Give the extent of all Plasmodium falciparum-infected red blood cells.
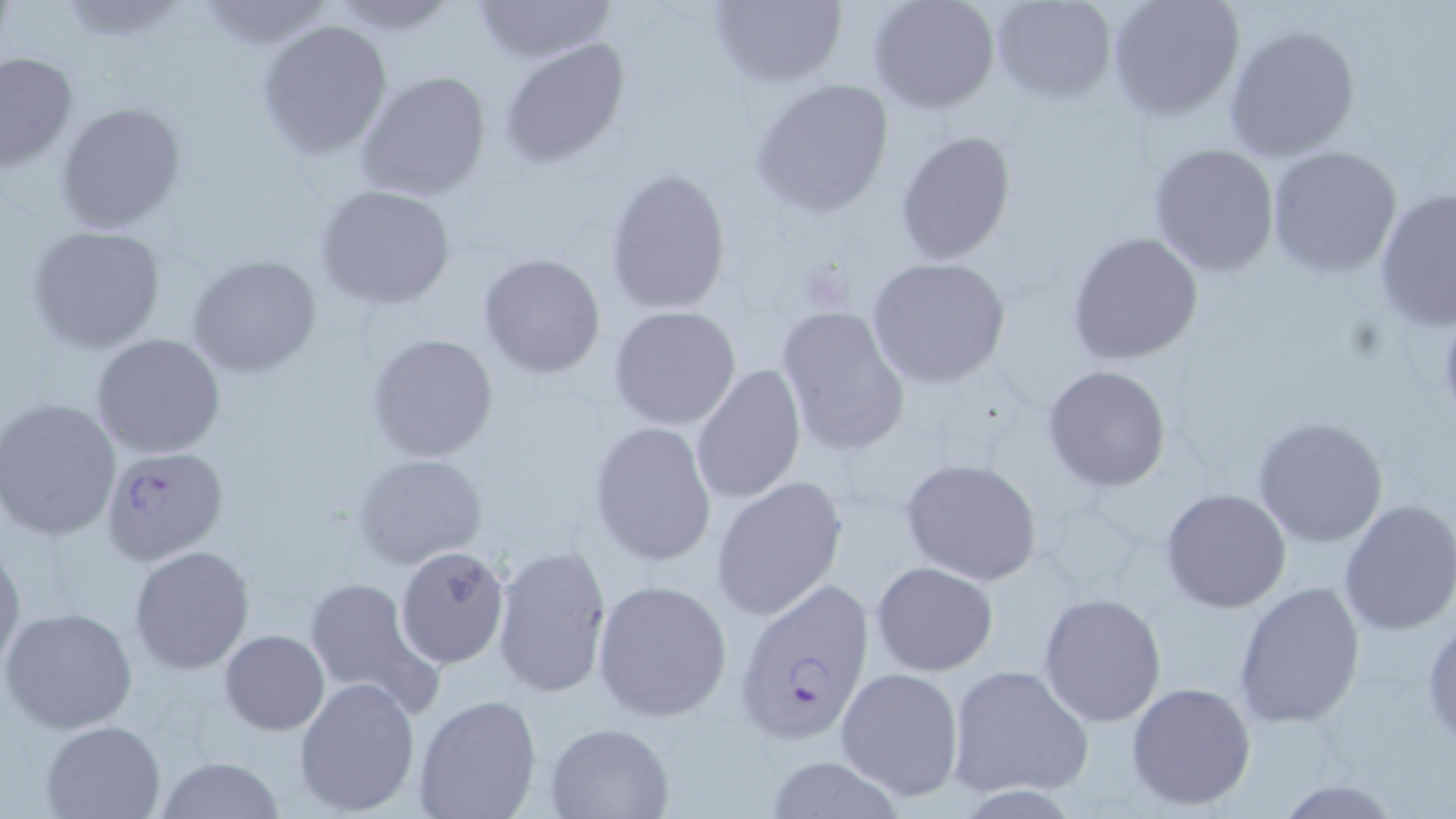

Approximate bounding boxes as (x1,y1)-(x2,y2) corner pairs in pixels.
Plasmodium falciparum-infected red blood cells: (101,447)-(230,567), (733,580)-(879,746).

slide-level diagnosis = Plasmodium falciparum
modality = optical microscopy
preparation = thin blood film
image size = 1456×819 pixels
stain = May-Grünwald-Giemsa
magnification = 1000x
field of view = one of a larger specimen
uninfected red blood cell locations = approximate bounding boxes as (x1,y1)-(x2,y2) corner pairs in pixels: (470,0)-(618,62), (708,0)-(847,87), (869,0)-(999,113), (991,0)-(1115,102), (1106,0)-(1245,121), (196,1)-(337,51), (322,1)-(460,35), (258,19)-(392,158), (1222,24)-(1362,163), (498,39)-(630,170), (0,52)-(80,175), (357,70)-(491,202), (750,78)-(896,218), (55,101)-(187,234), (895,129)-(1018,264), (1148,142)-(1280,276), (1266,147)-(1404,279), (604,167)-(734,314), (315,184)-(457,310), (1374,187)-(1456,330), (27,225)-(166,353), (1066,231)-(1207,365), (477,253)-(606,379), (188,254)-(322,377), (867,258)-(1011,389), (609,305)-(743,430), (774,308)-(911,457), (1430,313)-(1456,418), (365,332)-(498,463), (92,333)-(226,458), (691,364)-(807,506), (1042,364)-(1172,492), (0,397)-(121,542), (1251,415)-(1391,548), (588,421)-(716,566), (354,453)-(488,571), (898,457)-(1044,588), (711,476)-(847,621), (1160,488)-(1291,613), (1336,498)-(1456,637), (0,541)-(24,675), (493,543)-(613,700), (395,544)-(510,669), (129,546)-(254,674), (871,561)-(998,676), (302,575)-(443,718), (593,580)-(733,723), (1232,581)-(1366,729), (864,584)-(992,757), (1038,591)-(1168,726), (1,605)-(138,736), (1422,612)-(1456,749), (220,629)-(329,735), (946,664)-(1094,800), (834,666)-(965,800), (293,675)-(421,817), (1125,680)-(1255,811), (412,693)-(542,819), (41,719)-(167,818), (544,721)-(675,817), (155,755)-(286,819), (761,755)-(908,819), (1272,779)-(1404,817)